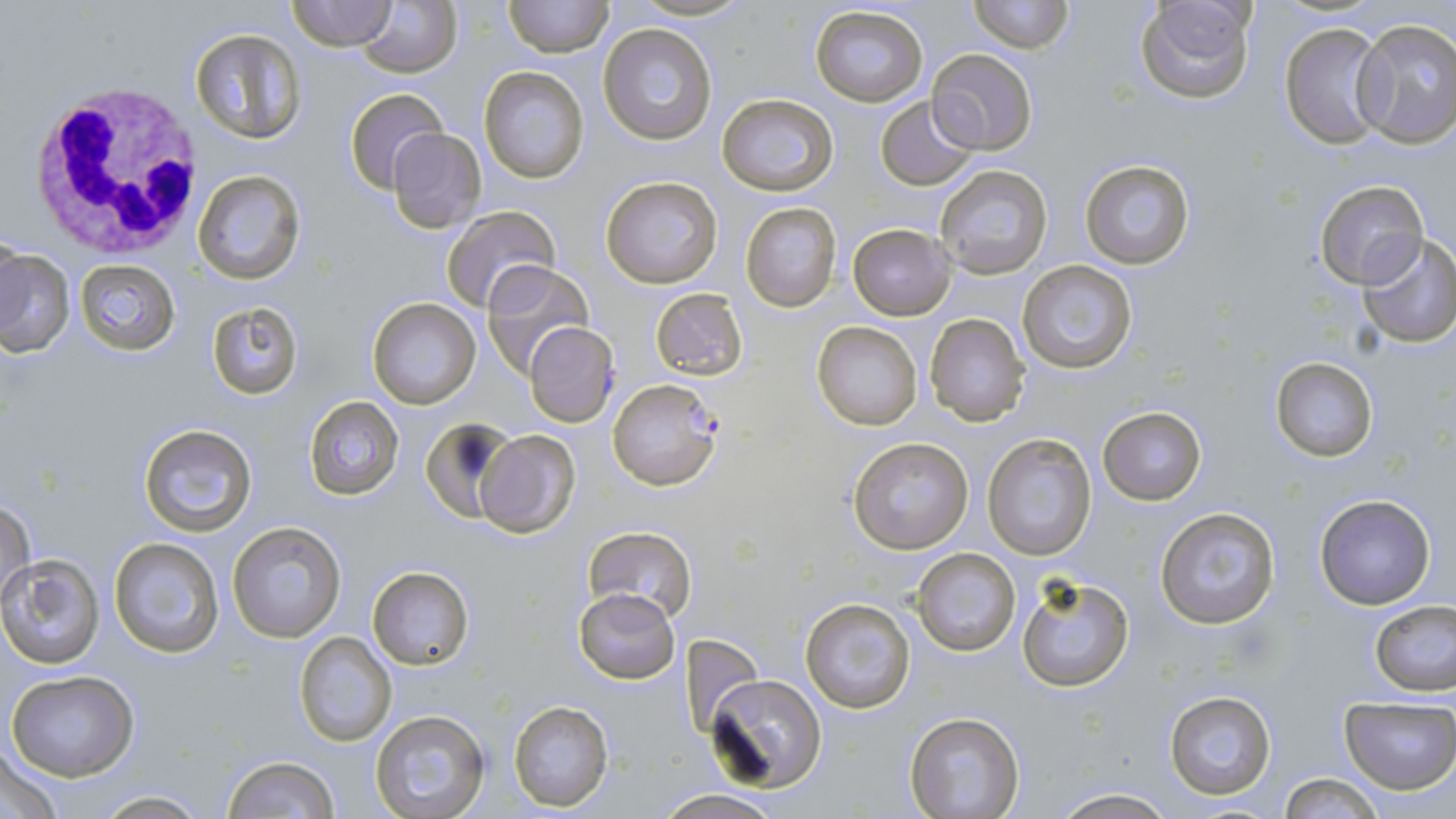
slide-level diagnosis = Plasmodium falciparum
field of view = single
Plasmodium falciparum-infected red blood cell locations = approximate bounding boxes as (x1,y1)-(x2,y2) corner pairs in pixels: (607,379)-(723,492)
magnification = 1000x
white blood cell locations = approximate bounding boxes as (x1,y1)-(x2,y2) corner pairs in pixels: (23,81)-(206,258)
image size = 1456×819 pixels
uninfected red blood cell locations = approximate bounding boxes as (x1,y1)-(x2,y2) corner pairs in pixels: (288,0)-(396,50), (354,0)-(462,78), (503,0)-(612,57), (628,0)-(752,22), (970,0)-(1072,53), (1135,0)-(1257,104), (809,4)-(929,108), (1351,18)-(1456,146), (1280,21)-(1389,148), (598,22)-(718,145), (189,28)-(306,143), (929,48)-(1037,156), (480,66)-(588,183), (346,89)-(446,192), (716,93)-(837,196), (875,95)-(980,190), (387,128)-(486,231), (1079,159)-(1196,270), (934,165)-(1053,278), (191,169)-(306,286), (599,174)-(723,289), (1313,179)-(1429,289), (738,201)-(843,313), (441,205)-(562,315), (847,223)-(955,319), (1356,232)-(1456,347), (0,246)-(76,360), (76,259)-(181,355), (1019,259)-(1137,374), (480,262)-(595,379), (650,288)-(748,380), (368,297)-(482,408), (208,303)-(302,398), (924,313)-(1031,426), (812,320)-(923,431), (524,322)-(619,426), (1270,357)-(1378,460), (303,396)-(404,500), (1097,406)-(1207,504), (421,419)-(519,522), (138,423)-(257,536), (472,427)-(580,536), (984,434)-(1095,560), (847,436)-(974,556), (1315,493)-(1436,609), (0,498)-(36,609), (1154,504)-(1281,629), (227,519)-(346,643), (583,526)-(696,622), (110,537)-(224,657), (912,547)-(1020,658), (1,556)-(103,668), (368,566)-(475,671), (1016,572)-(1135,692), (573,588)-(681,683), (801,597)-(917,713), (1369,601)-(1455,698), (294,632)-(396,746), (681,632)-(763,738), (7,670)-(138,780), (706,673)-(827,792), (1165,690)-(1276,801), (508,699)-(612,812), (1339,699)-(1456,793), (369,709)-(492,819), (906,713)-(1026,819), (1,743)-(65,818), (222,756)-(342,818), (1276,772)-(1386,818), (1049,787)-(1179,819), (658,790)-(780,819), (91,791)-(210,817)
modality = optical microscopy
preparation = thin blood smear
stain = May-Grünwald-Giemsa